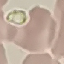

result = negative for malaria parasites
image type = cell patch, automatically extracted from a larger field of view and resized to 64 × 64 pixels
stain = Giemsa
capture = smartphone through the microscope eyepiece
preparation = thin smear